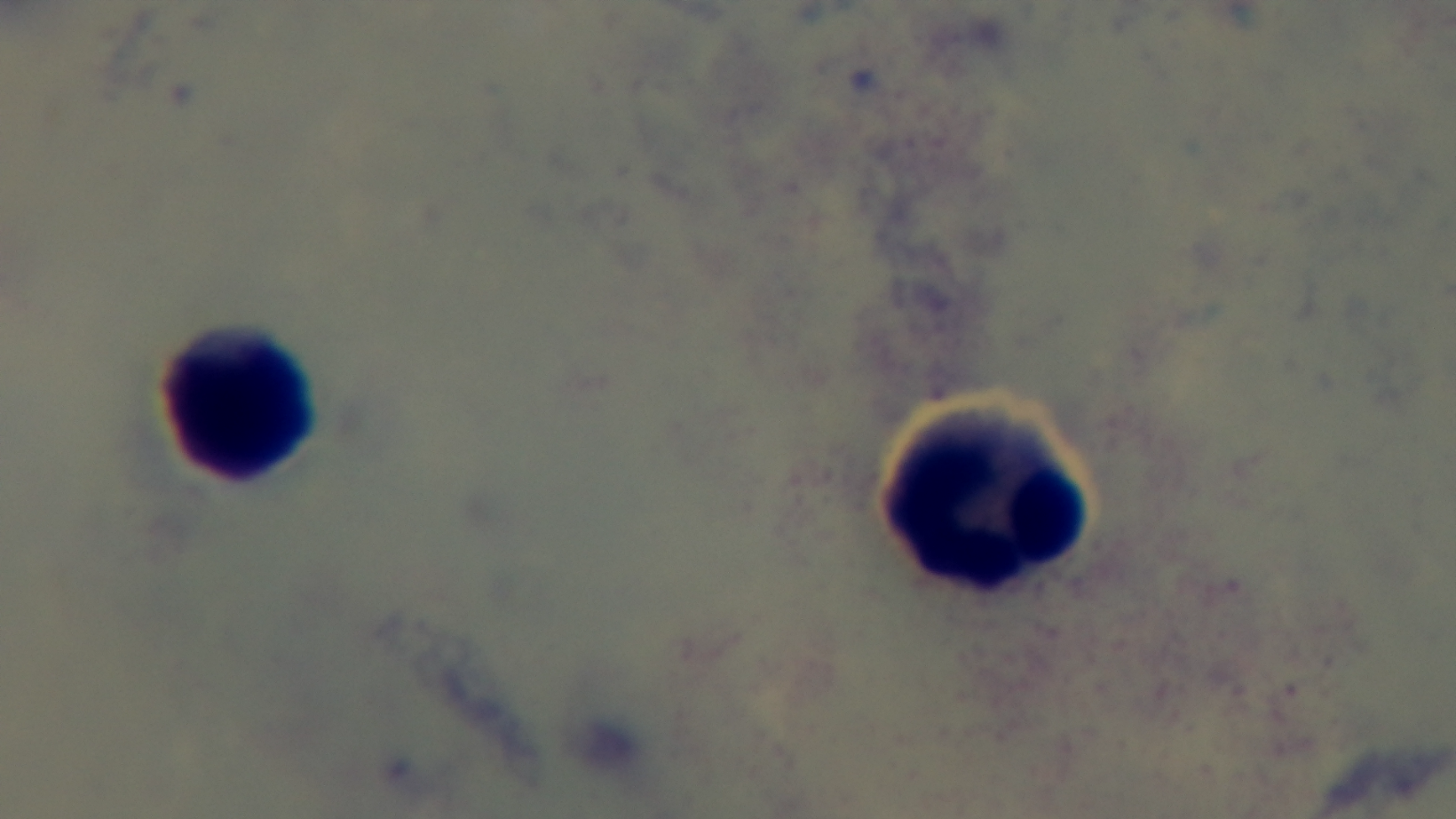 Photomicrograph. Preparation: thick. Single field of view. Malaria status: uninfected. Oil-immersion objective, 100x. Giemsa-stained. Captured with a mounted 4K digital camera.